Outline platelets.
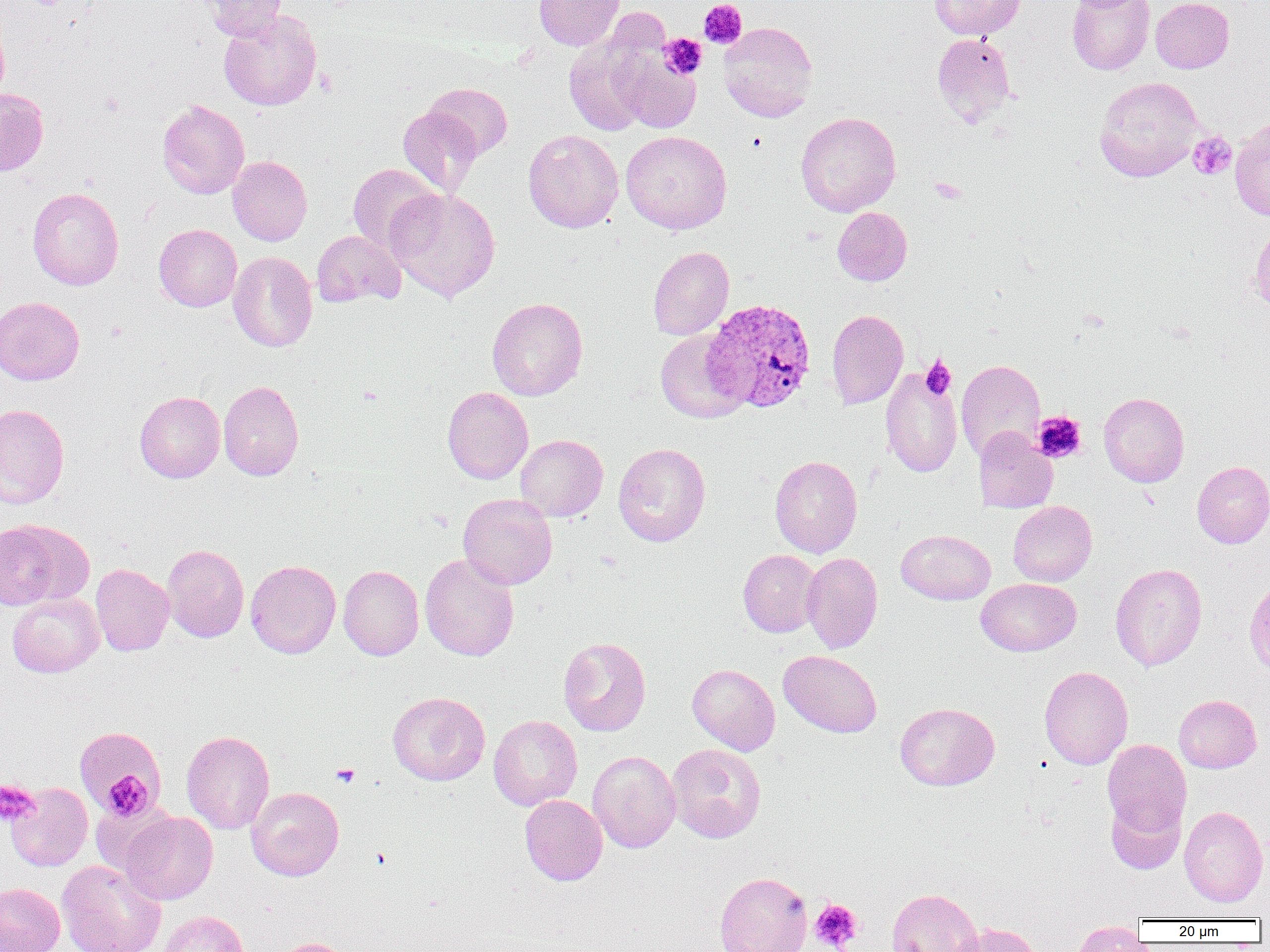
Approximate bounding boxes as [x1, y1, x2, y2] in pixels.
Platelets: [698, 0, 748, 49], [659, 34, 707, 80], [1188, 131, 1237, 180], [747, 133, 767, 153], [921, 356, 956, 399], [1032, 411, 1086, 463], [332, 763, 360, 787], [100, 770, 155, 820], [0, 780, 38, 827], [370, 848, 392, 871], [810, 899, 862, 951].

Uninfected red blood cell locations: [202, 0, 287, 42], [533, 0, 624, 50], [929, 0, 1026, 40], [1067, 0, 1154, 75], [1151, 0, 1234, 73], [219, 10, 322, 111], [0, 16, 9, 107], [718, 21, 818, 122], [563, 33, 656, 136], [932, 33, 1017, 126], [612, 46, 701, 134], [1095, 76, 1204, 182], [424, 83, 512, 160], [0, 87, 49, 175], [157, 99, 250, 199], [398, 106, 482, 197], [795, 112, 901, 217], [1230, 120, 1270, 220], [522, 129, 624, 233], [621, 130, 732, 234], [228, 156, 312, 245], [347, 163, 441, 255], [27, 187, 124, 290], [386, 187, 502, 302], [832, 207, 912, 286], [1250, 220, 1270, 316], [154, 224, 242, 311], [312, 230, 405, 308], [647, 246, 734, 340], [228, 251, 317, 352], [0, 296, 85, 385], [487, 297, 587, 400], [826, 309, 908, 410], [655, 329, 749, 423], [956, 359, 1045, 462], [880, 366, 962, 478], [218, 380, 304, 481], [442, 386, 533, 484], [135, 391, 225, 483], [1099, 392, 1189, 487], [0, 403, 70, 509], [974, 427, 1057, 512], [515, 434, 608, 521], [612, 443, 711, 547], [770, 455, 862, 557], [1192, 461, 1270, 548], [457, 493, 558, 589], [1008, 500, 1097, 586], [0, 519, 93, 609], [896, 529, 995, 604], [162, 544, 249, 642], [738, 549, 822, 637], [801, 552, 883, 654], [419, 553, 520, 661], [245, 559, 341, 658], [1110, 563, 1207, 671], [91, 564, 174, 656], [338, 565, 424, 660], [975, 578, 1081, 656], [1244, 578, 1270, 679], [7, 592, 104, 678], [558, 636, 651, 736], [778, 650, 882, 737], [687, 664, 780, 755], [1039, 666, 1133, 769], [388, 691, 490, 785], [1174, 694, 1262, 773], [894, 702, 999, 790], [488, 714, 582, 810], [74, 727, 167, 817], [181, 730, 275, 833], [1102, 739, 1191, 836], [667, 743, 766, 842], [588, 751, 680, 853], [6, 783, 93, 871], [247, 787, 344, 880], [520, 795, 607, 885], [1106, 795, 1185, 873], [1179, 805, 1268, 907], [120, 810, 217, 905], [57, 859, 166, 952], [714, 871, 812, 952], [0, 882, 65, 952], [886, 888, 983, 952], [157, 910, 249, 952], [1070, 921, 1148, 951], [952, 922, 1043, 952], [272, 938, 351, 952]. Plasmodium vivax-infected red blood cell locations: [701, 298, 817, 413]. Slide-level diagnosis: Plasmodium vivax. Image is 1270×952 pixels. Thin blood film. Single field of view. Optical microscopy. 1000x magnification.